State which parasite is depicted.
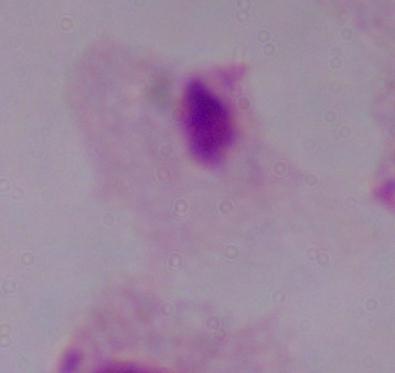
This is a trichomonad.

Summary:
  - Modality: micrograph
  - Magnification: 1000x